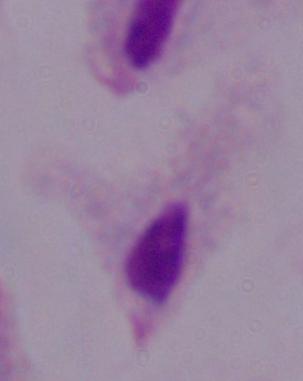
Captured at 1000x magnification. Micrograph. A trichomonad is shown.